Classify this cell by malaria status.
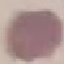
Uninfected.

Summary:
  - Stain: Giemsa
  - Image type: cell patch, automatically extracted from a larger field of view and resized to 64 × 64 pixels
  - Capture: smartphone through the microscope eyepiece
  - Preparation: thin blood smear